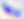

{
  "identification": "Toxoplasma gondii",
  "magnification": "400x",
  "modality": "micrograph"
}